Classify this cell by malaria status.
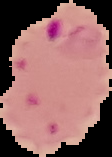

It is parasitized.

Image is 112×157 pixels. Segmented cell region on a black background. From a thin blood film.